Give the extent of all Plasmodium falciparum-infected red blood cells.
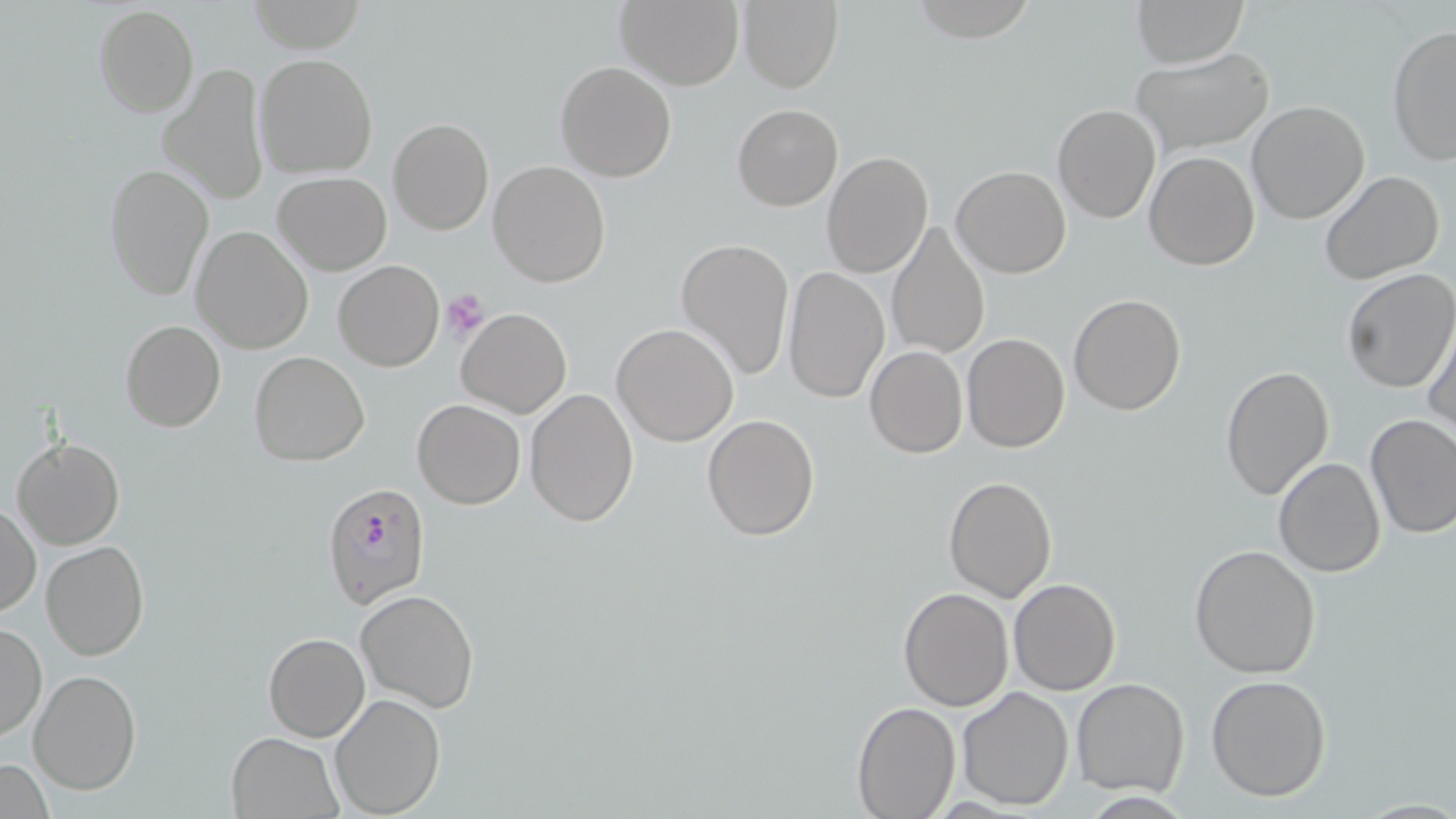

Approximate bounding boxes as (x1,y1)-(x2,y2) corner pairs in pixels.
Plasmodium falciparum-infected red blood cells: (322,482)-(431,608).

slide-level diagnosis = Plasmodium falciparum
field of view = single
platelet locations = approximate bounding boxes as (x1,y1)-(x2,y2) corner pairs in pixels: (441,288)-(491,340)
preparation = thin blood film
uninfected red blood cell locations = approximate bounding boxes as (x1,y1)-(x2,y2) corner pairs in pixels: (248,0)-(366,53), (615,0)-(744,89), (738,0)-(845,93), (908,0)-(1037,40), (1132,0)-(1249,68), (94,4)-(198,116), (1387,25)-(1456,164), (1132,46)-(1275,156), (255,53)-(378,179), (554,60)-(677,183), (158,62)-(271,206), (1246,100)-(1370,224), (731,103)-(843,211), (1052,103)-(1160,223), (387,118)-(494,235), (822,150)-(934,279), (1144,151)-(1259,271), (488,159)-(611,288), (103,164)-(213,299), (952,164)-(1071,278), (1319,169)-(1446,283), (273,172)-(391,274), (885,222)-(991,359), (190,225)-(314,354), (675,236)-(796,379), (334,260)-(444,371), (782,265)-(888,405), (1339,268)-(1455,394), (1067,293)-(1187,416), (456,308)-(572,418), (1425,316)-(1456,442), (120,320)-(226,433), (612,323)-(740,446), (962,333)-(1070,453), (864,346)-(968,459), (248,351)-(369,465), (1222,365)-(1334,502), (525,385)-(638,526), (412,398)-(526,509), (702,413)-(819,540), (1365,413)-(1456,538), (12,436)-(124,550), (1272,458)-(1386,577), (942,476)-(1057,602), (1,503)-(40,619), (41,540)-(151,660), (1189,545)-(1322,678), (1007,578)-(1121,695), (898,588)-(1014,710), (356,590)-(481,712), (0,621)-(46,742), (263,633)-(369,742), (29,670)-(140,794), (1205,674)-(1332,802), (1071,676)-(1190,797), (956,686)-(1074,811), (330,693)-(445,818), (851,700)-(960,818), (227,733)-(343,818), (1,758)-(54,818)
magnification = 1000x
modality = optical microscopy
stain = May-Grünwald-Giemsa
image size = 1456×819 pixels